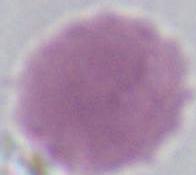

magnification = 1000x
modality = photomicrograph
identification = erythrocyte